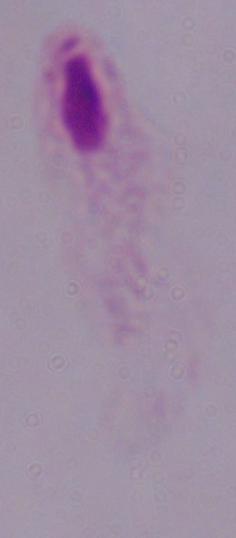 Captured at 1000x magnification. Micrograph. A trichomonad is seen.